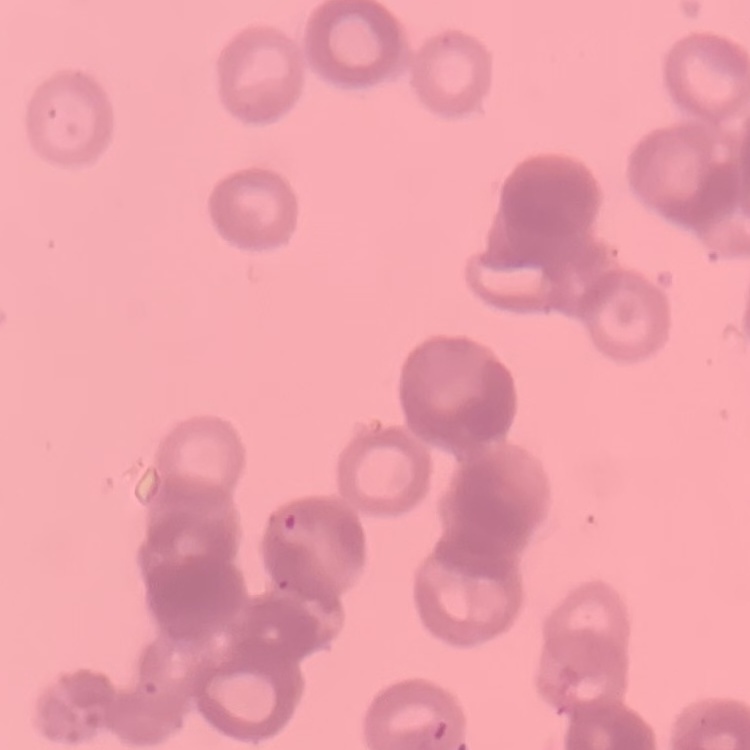
erythrocyte morphology = rouleaux formation
preparation = thin blood smear
image type = square crop of a larger photomicrograph
stain = Field's or Giemsa